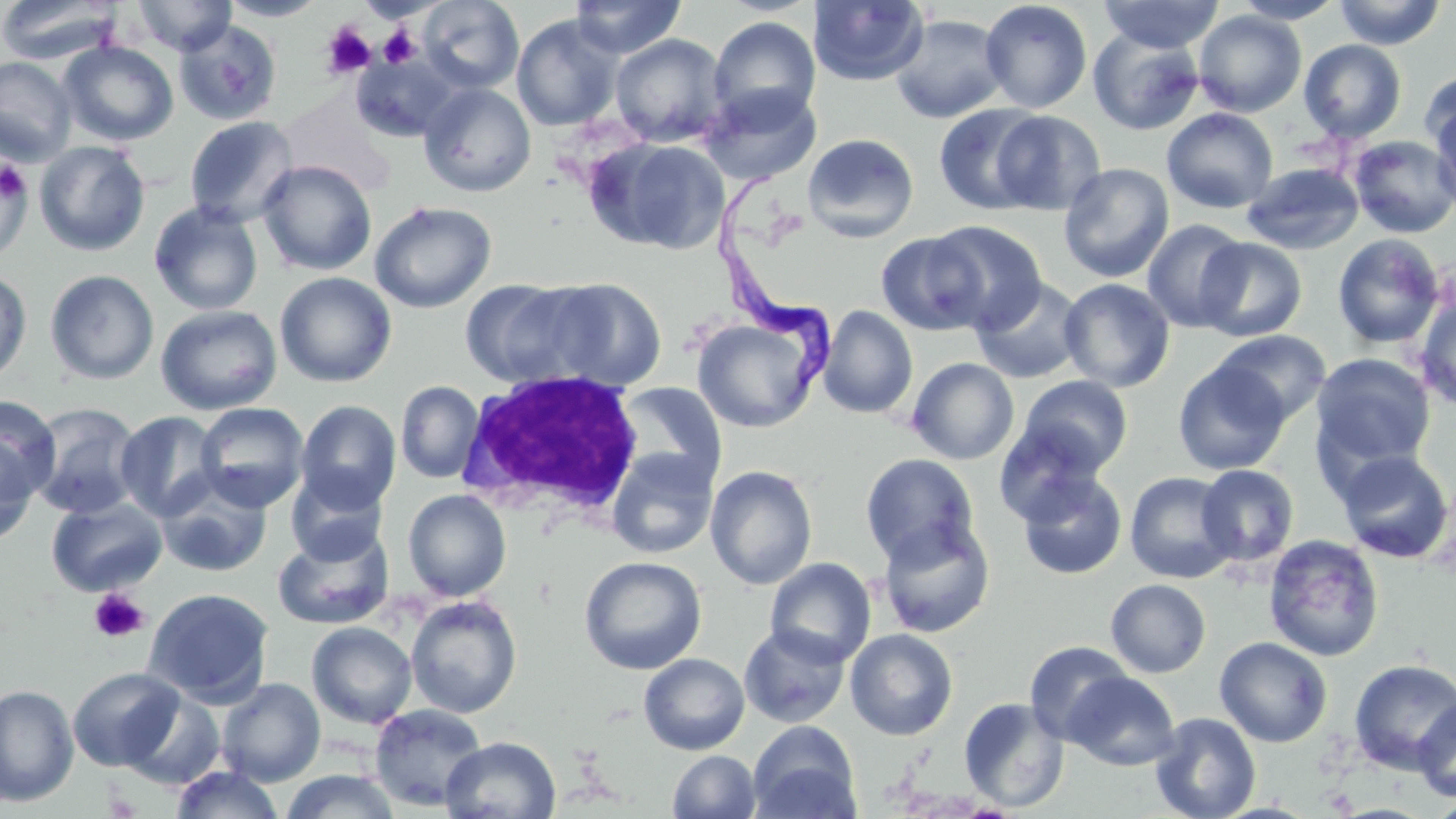
Approximate bounding boxes as (x1, y1, x2, y2) in pixels. Platelet locations: (321, 22, 376, 78), (379, 26, 420, 67), (0, 159, 29, 202), (89, 588, 149, 643), (104, 790, 141, 817). Uninfected red blood cell locations: (133, 0, 236, 56), (218, 0, 329, 21), (418, 0, 524, 94), (569, 0, 687, 59), (979, 0, 1093, 113), (1097, 0, 1224, 54), (1230, 0, 1346, 24), (1332, 0, 1446, 49), (0, 1, 123, 65), (808, 1, 930, 86), (1192, 10, 1307, 117), (511, 14, 623, 131), (889, 14, 1010, 124), (708, 16, 822, 127), (175, 22, 281, 126), (1088, 29, 1205, 136), (609, 33, 730, 147), (1298, 39, 1407, 143), (59, 40, 178, 146), (352, 52, 461, 142), (0, 56, 77, 163), (1418, 69, 1456, 158), (419, 83, 537, 197), (698, 83, 821, 185), (278, 89, 394, 195), (1428, 93, 1456, 212), (934, 104, 1050, 216), (1161, 108, 1278, 214), (990, 110, 1106, 215), (184, 116, 299, 228), (802, 133, 919, 242), (1349, 135, 1456, 238), (586, 136, 731, 255), (34, 140, 151, 256), (0, 158, 33, 263), (257, 160, 377, 276), (1242, 162, 1365, 255), (1058, 163, 1175, 283), (369, 201, 497, 314), (148, 202, 264, 316), (1141, 218, 1249, 333), (926, 220, 1047, 333), (875, 231, 989, 335), (1332, 234, 1445, 350), (1195, 237, 1307, 342), (0, 267, 33, 387), (44, 270, 159, 385), (274, 272, 397, 388), (542, 277, 667, 391), (459, 278, 595, 389), (971, 278, 1087, 384), (1058, 278, 1176, 392), (1415, 292, 1456, 412), (155, 304, 282, 416), (818, 305, 918, 419), (691, 314, 824, 433), (1212, 330, 1332, 425), (1310, 352, 1436, 475), (906, 357, 1020, 464), (1174, 361, 1290, 475), (1016, 376, 1135, 479), (395, 381, 485, 484), (616, 381, 727, 489), (0, 395, 61, 504), (295, 400, 401, 513), (194, 402, 310, 513), (26, 403, 144, 520), (114, 410, 224, 521), (994, 424, 1104, 526), (0, 436, 37, 547), (606, 448, 719, 559), (1335, 449, 1454, 564), (860, 454, 981, 567), (705, 465, 818, 590), (1195, 465, 1299, 567), (1015, 467, 1128, 580), (285, 470, 388, 565), (1124, 471, 1239, 583), (156, 473, 273, 577), (402, 489, 511, 602), (46, 496, 168, 597), (877, 517, 996, 638), (272, 527, 394, 629), (1263, 534, 1385, 662), (579, 556, 707, 675), (765, 557, 877, 667), (1106, 579, 1211, 678), (142, 587, 274, 706), (405, 595, 522, 718), (306, 621, 418, 729), (739, 624, 851, 728), (845, 628, 958, 741), (1214, 636, 1333, 747), (1025, 641, 1136, 745), (638, 653, 750, 755), (1348, 659, 1456, 774), (67, 667, 184, 771), (1065, 671, 1181, 771), (217, 678, 326, 786), (0, 684, 78, 807), (958, 697, 1070, 813), (1412, 699, 1456, 802), (369, 704, 488, 812), (1150, 712, 1262, 819), (748, 720, 861, 819), (439, 736, 561, 819), (667, 750, 761, 819), (170, 765, 286, 819), (280, 768, 401, 819), (1430, 797, 1456, 819). White blood cell locations: (458, 368, 647, 521). Trypanosoma brucei locations: (706, 167, 839, 403). Slide-level diagnosis: Trypanosoma brucei. Thin blood smear. Image is 1456×819 pixels. May-Grünwald-Giemsa stain. One field of a larger specimen. 1000x magnification. Optical microscopy.